Comment on the morphology of the red blood cells.
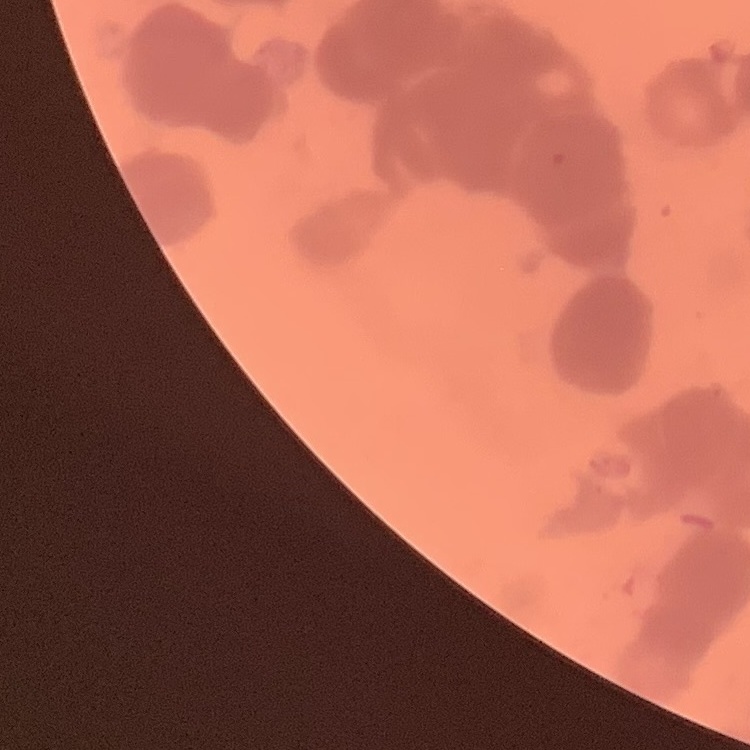

They show rouleaux formation.

stain = Field's or Giemsa
image type = one tile cut from a larger photomicrograph
preparation = thin blood film